Identify the parasite.
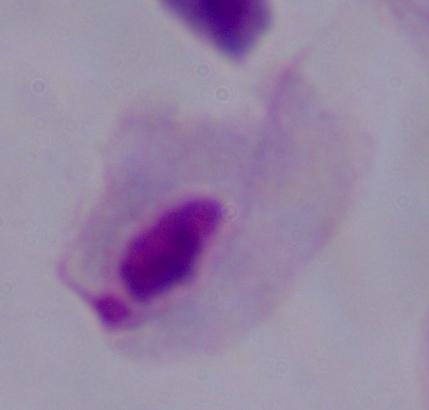
This is a trichomonad.

Captured at 1000x magnification. Photomicrograph.